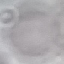

malaria status = uninfected
preparation = thin blood film
image type = cell patch, automatically extracted from a larger field of view and resized to 64 × 64 pixels
capture = smartphone through the microscope eyepiece
stain = Giemsa